State which parasite is depicted.
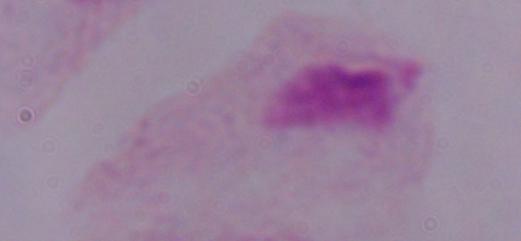
This is a trichomonad.

1000x magnification. Micrograph.